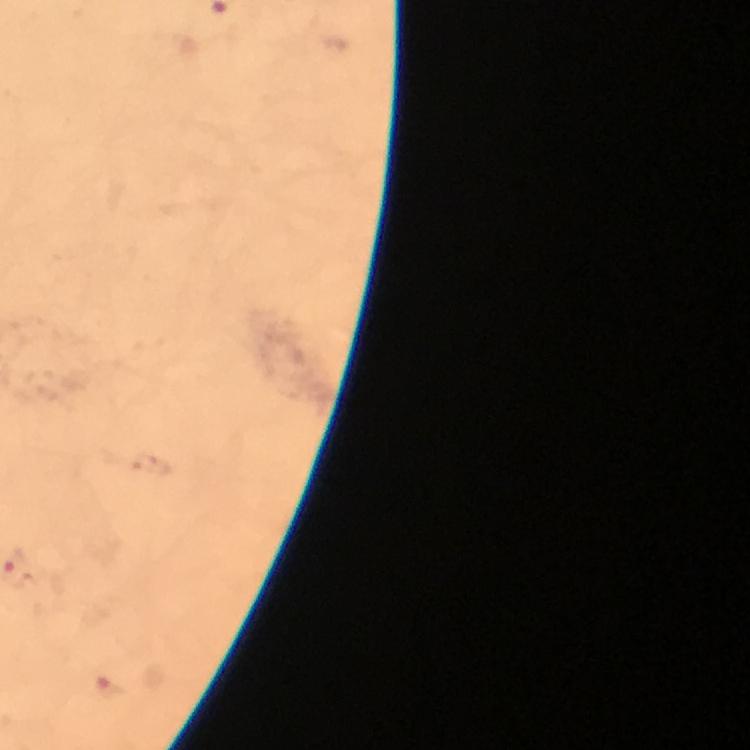
Approximate centers as [x, y] in pixels.
Summary:
  - Malaria parasite locations: [108, 689]
  - Capture: smartphone mounted on the microscope
  - Cropped from: one field of view
  - Image size: 750×750 pixels
  - Preparation: thick smear
  - Stain: Giemsa
  - Magnification: 100x
  - Immersion oil: applied
  - Context: from a malaria diagnostic workup